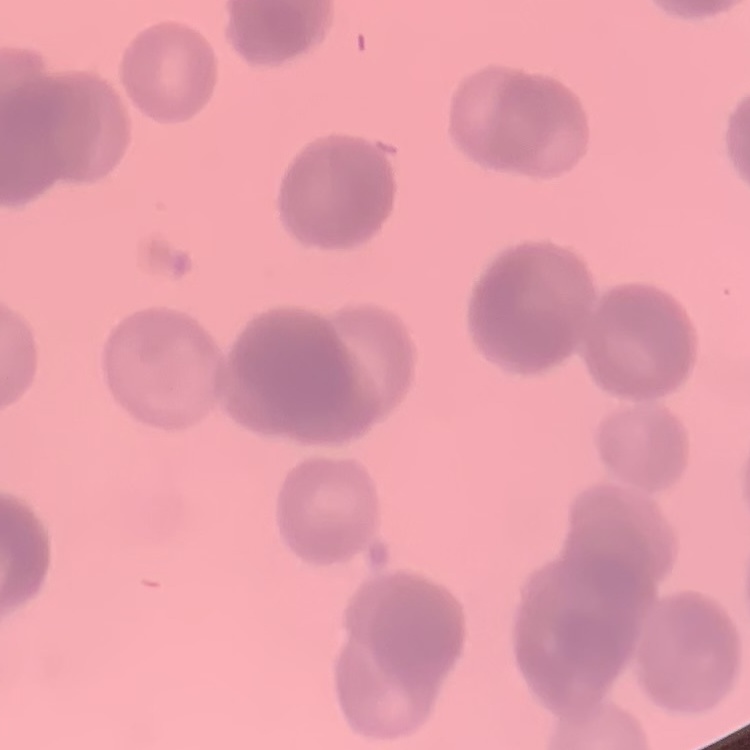

Summary:
  - Erythrocyte morphology: rouleaux formation
  - Stain: Field's or Giemsa
  - Image type: square crop of a larger photomicrograph
  - Preparation: thin blood film